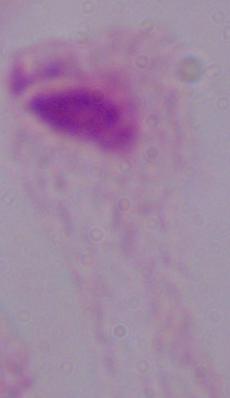
Summary:
  - Identification: trichomonad
  - Magnification: 1000x
  - Modality: photomicrograph